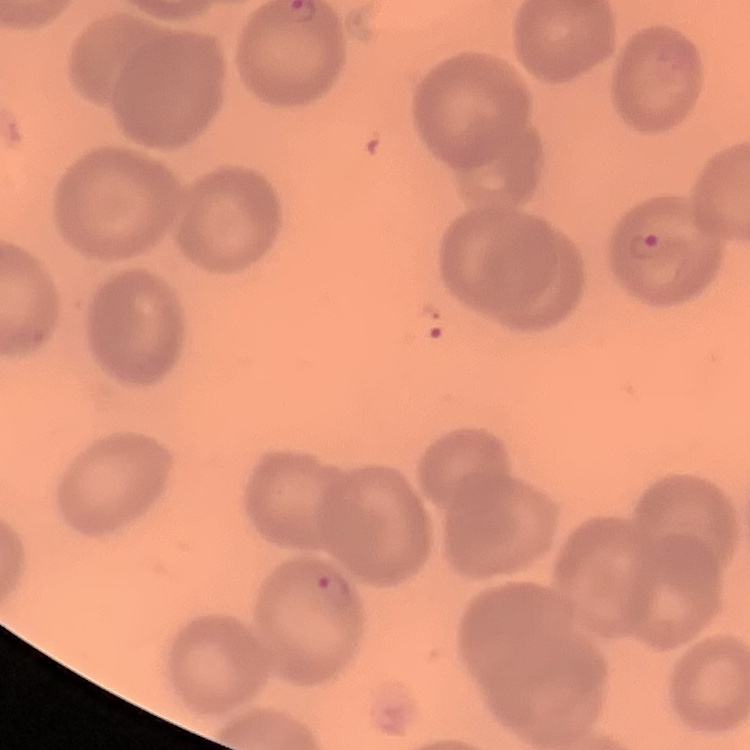
Summary:
  - Red blood cell morphology: no rouleaux formation
  - Image type: one tile cut from a larger photomicrograph
  - Preparation: thin blood smear
  - Stain: Field's or Giemsa